Locate and identify every blood parasite.
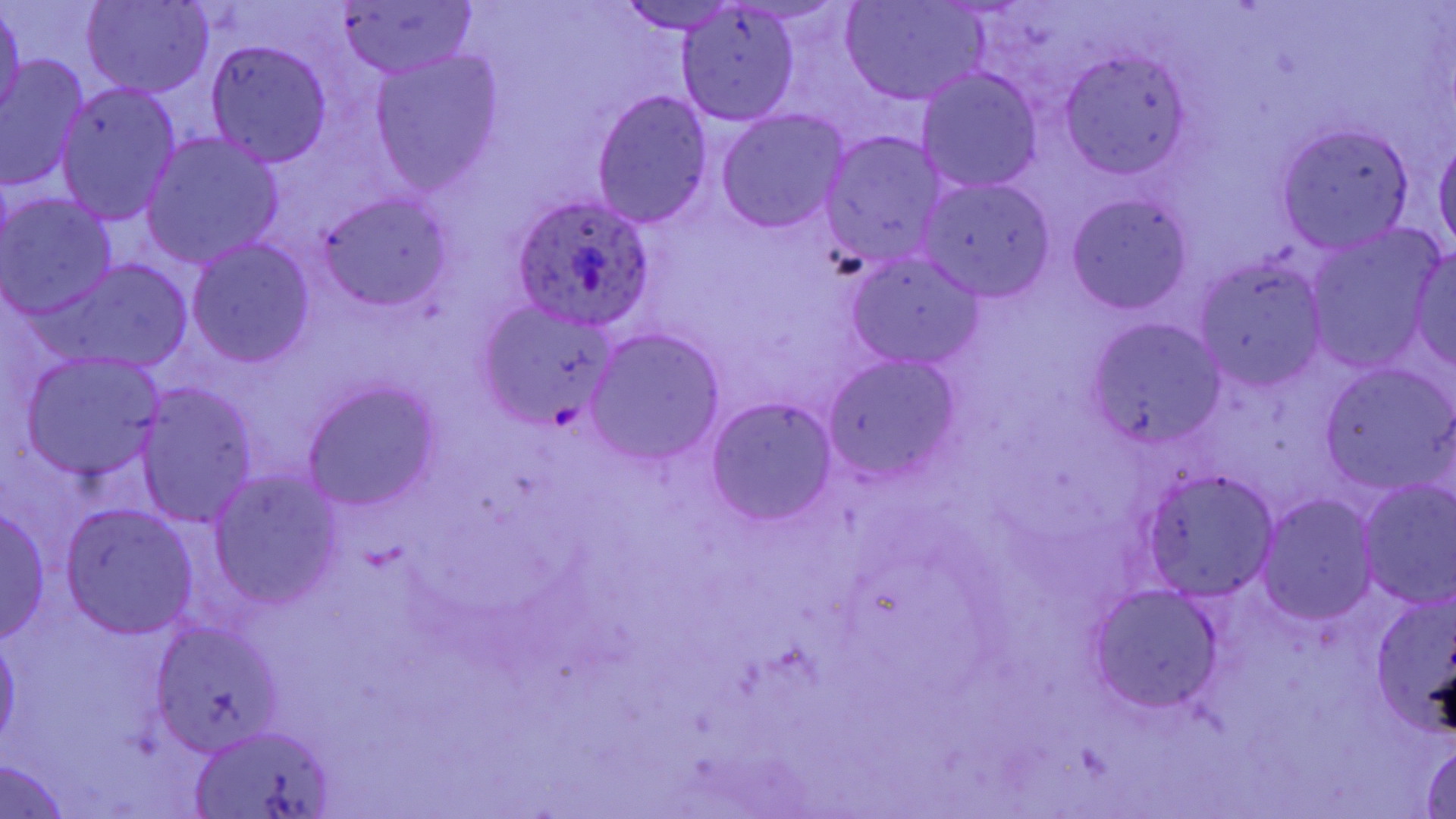

Approximate bounding boxes as (x1, y1, x2, y2) in pixels.
Plasmodium ovale-infected red blood cells: (511, 197, 659, 332).
No Plasmodium falciparum, Plasmodium malariae, Plasmodium vivax, Babesia divergens, or Trypanosoma brucei observed.

Summary:
  - Uninfected red blood cell locations: (83, 0, 213, 98), (841, 0, 988, 106), (0, 2, 25, 127), (335, 2, 475, 78), (615, 2, 743, 34), (675, 6, 800, 126), (206, 41, 333, 166), (1060, 52, 1191, 178), (371, 53, 502, 192), (1, 55, 91, 192), (917, 68, 1043, 192), (55, 81, 183, 225), (591, 90, 715, 228), (716, 109, 850, 235), (1279, 124, 1413, 250), (820, 131, 948, 269), (142, 133, 283, 267), (1434, 133, 1455, 258), (918, 176, 1055, 300), (1, 193, 118, 317), (315, 194, 455, 309), (1067, 194, 1192, 315), (1304, 231, 1439, 370), (188, 239, 316, 367), (1409, 250, 1456, 368), (845, 251, 985, 370), (1195, 257, 1330, 390), (53, 260, 192, 369), (474, 299, 621, 432), (1090, 318, 1226, 453), (587, 329, 725, 465), (22, 354, 168, 483), (821, 354, 964, 484), (1320, 365, 1454, 492), (303, 380, 442, 511), (135, 386, 258, 526), (706, 396, 839, 526), (209, 470, 345, 609), (1143, 470, 1279, 599), (1355, 480, 1456, 607), (1257, 494, 1377, 625), (60, 504, 200, 639), (0, 505, 52, 644), (1371, 582, 1456, 740), (1087, 585, 1225, 713), (152, 622, 286, 755), (0, 634, 21, 750), (192, 727, 336, 817), (1418, 739, 1456, 818), (0, 759, 75, 816)
  - Slide-level diagnosis: Plasmodium ovale
  - Field of view: one of a larger specimen
  - Stain: May-Grünwald-Giemsa
  - Preparation: thin blood smear
  - Modality: optical microscopy
  - Image size: 1456×819 pixels
  - Magnification: 1000x